Identify the parasite.
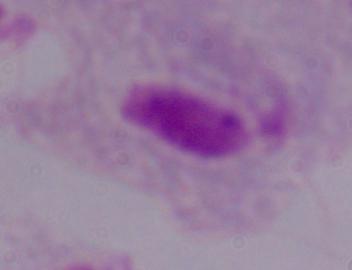

This is a trichomonad.

Captured at 1000x magnification. Photomicrograph.